Report the malaria status of this cell.
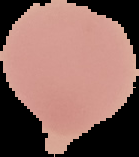

Uninfected.

Summary:
  - Image size: 139×157 pixels
  - Image type: segmented cell region on a black background
  - Preparation: thin blood film